Report the malaria status of this cell.
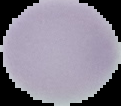
It is uninfected.

From a thin blood smear. The area outside the segmented cell region is set to black. Image is 121×106 pixels.